Assess this cell for malaria.
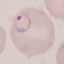
It is parasitized.

image_type: cell patch, automatically extracted from a larger field of view and resized to 64 × 64 pixels
preparation: thin blood smear
stain: Giemsa
capture: smartphone through the microscope eyepiece